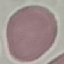
Summary:
  - Result: negative for malaria parasites
  - Stain: Giemsa
  - Image type: automatically extracted cell patch, resized to 64 × 64 pixels
  - Capture: smartphone camera at the microscope eyepiece
  - Preparation: thin smear